State which parasite is depicted.
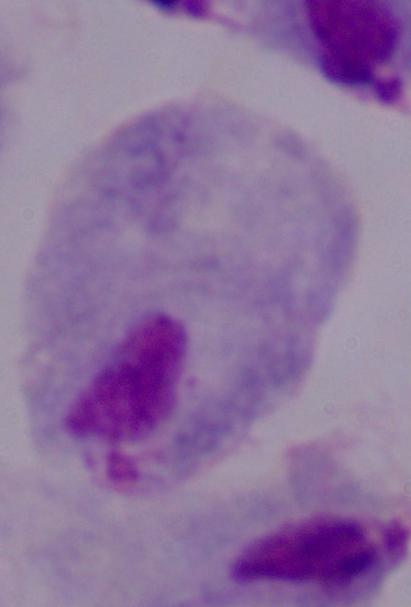

This is a trichomonad.

{
  "magnification": "1000x",
  "modality": "micrograph"
}